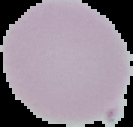
preparation: thin blood smear
result: negative for Plasmodium parasites
image_type: cell region segmented out of the field of view; surrounding area masked to black
image_size: 133×127 pixels